Assess the morphology of the erythrocytes.
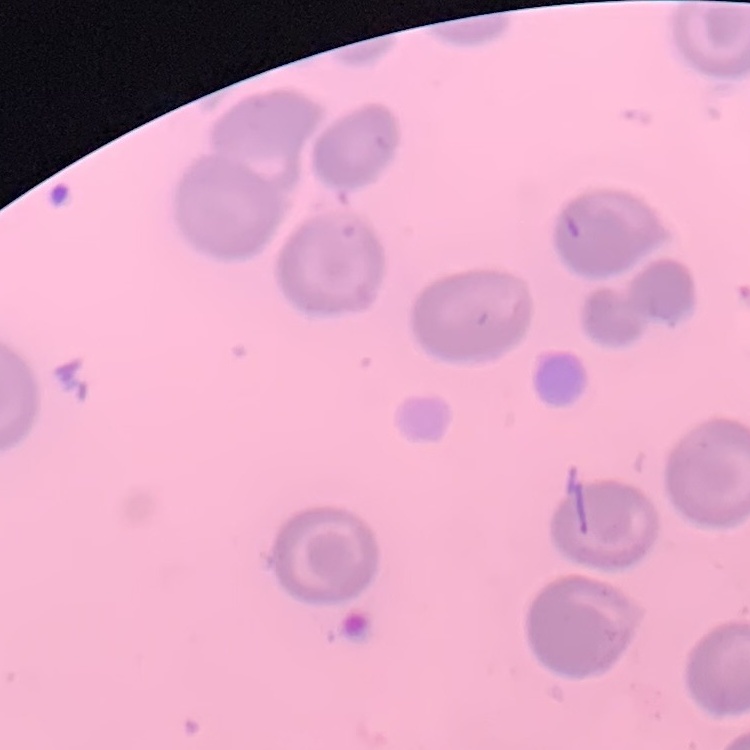

No rouleaux formation.

Summary:
  - Image type: one tile cut from a larger photomicrograph
  - Preparation: thin blood film
  - Stain: Field's or Giemsa